Outline every leukocyte.
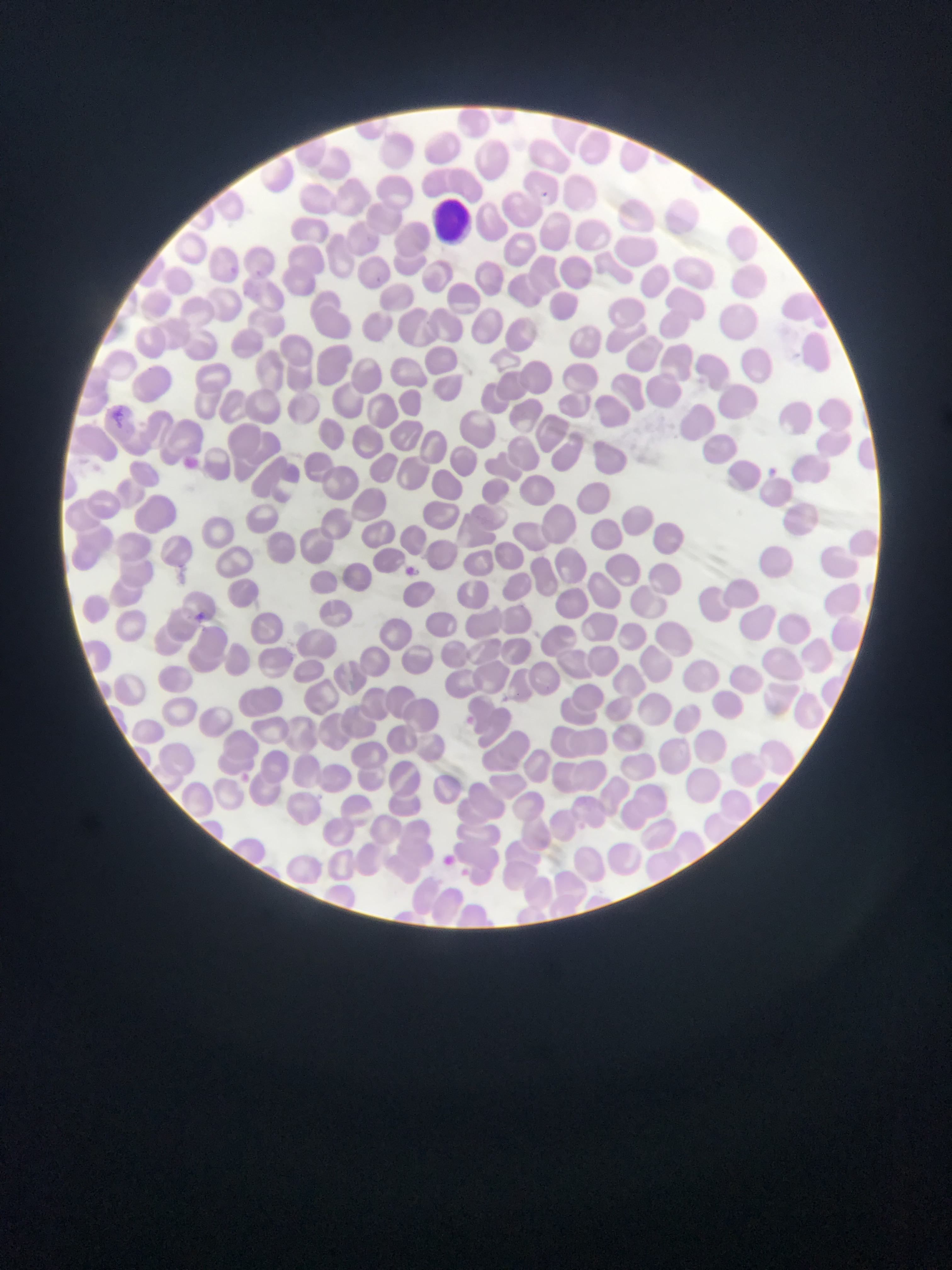
Approximate bounding boxes as (left, top, right, bottom) in pixels.
Leukocytes: (430, 198, 479, 233).

capture: mobile-phone photograph through a microscope
preparation: thin blood smear
country: Ghana
field_of_view: single
image_size: 952×1270 pixels
plasmodium_parasite_locations: 'approximate bounding boxes as (left, top, right, bottom) in pixels: (229, 263, 238, 275), (371, 269, 388, 284), (106, 405, 131, 423), (769, 465, 779, 478), (403, 562, 420, 577), (195, 611, 204, 627), (444, 853, 457, 868)'